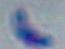

magnification = 1000x
identification = Toxoplasma gondii
modality = photomicrograph